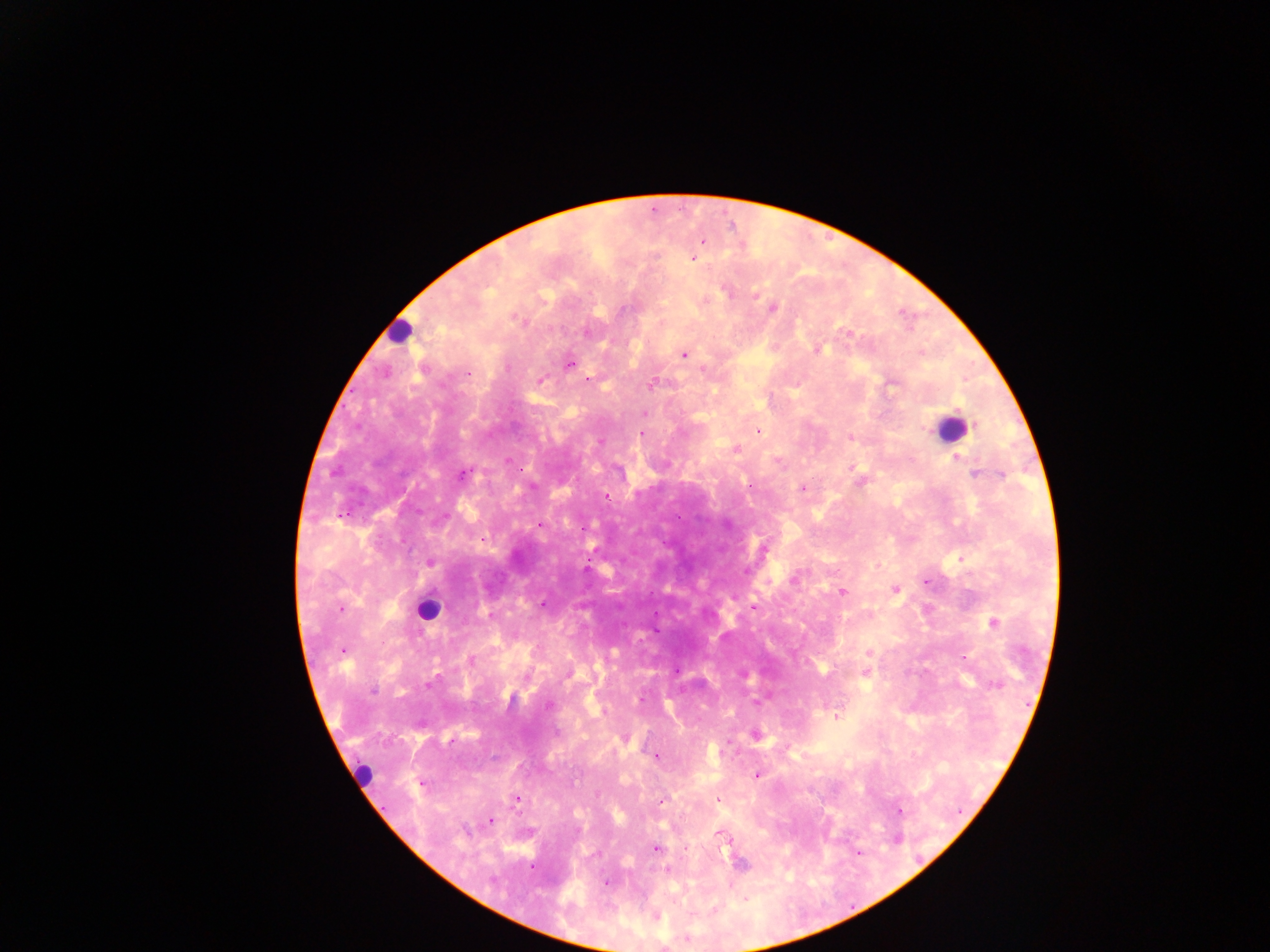
Approximate centers as (x, y) in pixels. Leukocyte locations (subset; some below the resolvable size): (400, 332), (949, 429), (427, 610), (363, 774). Plasmodium parasite locations: (702, 241), (692, 259), (727, 292), (756, 295), (705, 300), (773, 308), (622, 309), (518, 319), (587, 331), (848, 332), (818, 349), (684, 355), (569, 364), (508, 367), (424, 369), (468, 373), (588, 379), (541, 381), (652, 384), (892, 384), (645, 413), (758, 431), (641, 434), (850, 437), (600, 441), (735, 449), (958, 458), (507, 461), (777, 462), (963, 464), (853, 467), (520, 469), (974, 473), (462, 474), (1002, 475), (860, 481), (749, 484), (802, 488), (606, 498), (539, 525), (583, 529), (430, 563), (587, 569), (795, 578), (926, 582), (895, 590), (842, 592), (542, 604), (753, 608), (340, 609), (489, 615), (994, 623), (655, 630), (342, 651), (869, 652), (471, 660), (864, 673), (568, 674), (428, 684), (995, 685), (374, 690), (641, 699), (549, 705), (837, 717), (755, 735), (727, 740), (656, 756), (757, 775), (421, 784), (598, 794), (517, 799), (717, 800), (661, 802), (901, 811), (491, 821), (719, 834), (656, 849), (738, 863), (531, 867), (667, 869), (605, 882), (656, 918). Thick blood smear. Sample from Ghana. Single field of view. Mobile-phone photograph taken through the microscope. Image is 1270×952 pixels.